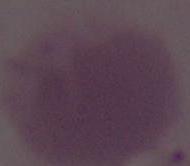

identification = red blood cell
magnification = 1000x
modality = micrograph